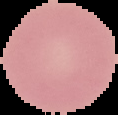
Summary:
  - Malaria status: uninfected
  - Image size: 118×115 pixels
  - Image type: segmented cell region with the area outside set to black
  - Preparation: thin blood smear